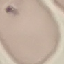
Summary:
  - Result: negative for malaria parasites
  - Capture: smartphone through the microscope eyepiece
  - Preparation: thin blood smear
  - Stain: Giemsa
  - Image type: automatically extracted cell patch, resized to 64 × 64 pixels